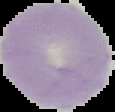

preparation = thin blood smear
image size = 115×112 pixels
malaria status = uninfected
image type = cell region segmented out of the field of view; surrounding area masked to black